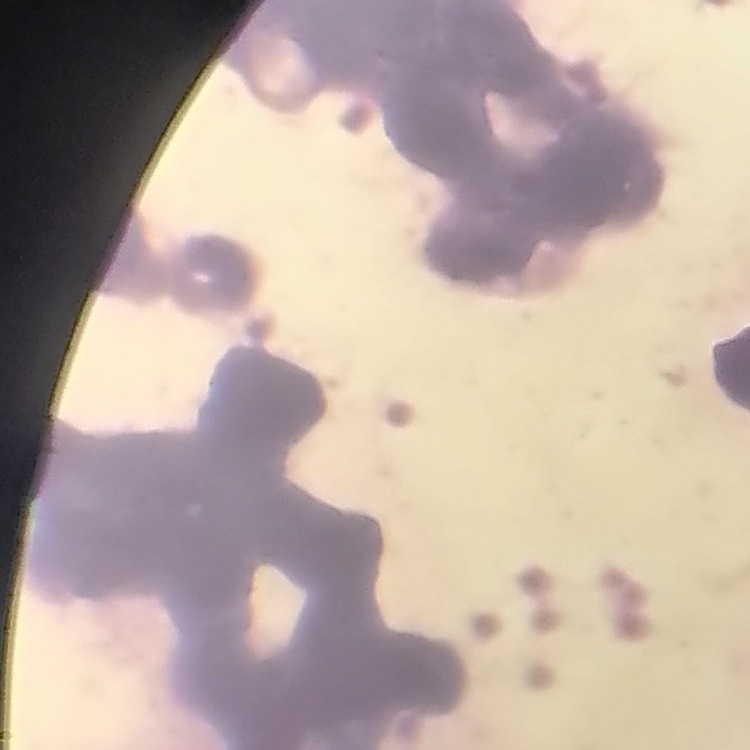
The erythrocytes exhibit rouleaux formation. Stained with either Field's or Giemsa. Thin blood film. One tile cut from a larger photomicrograph.